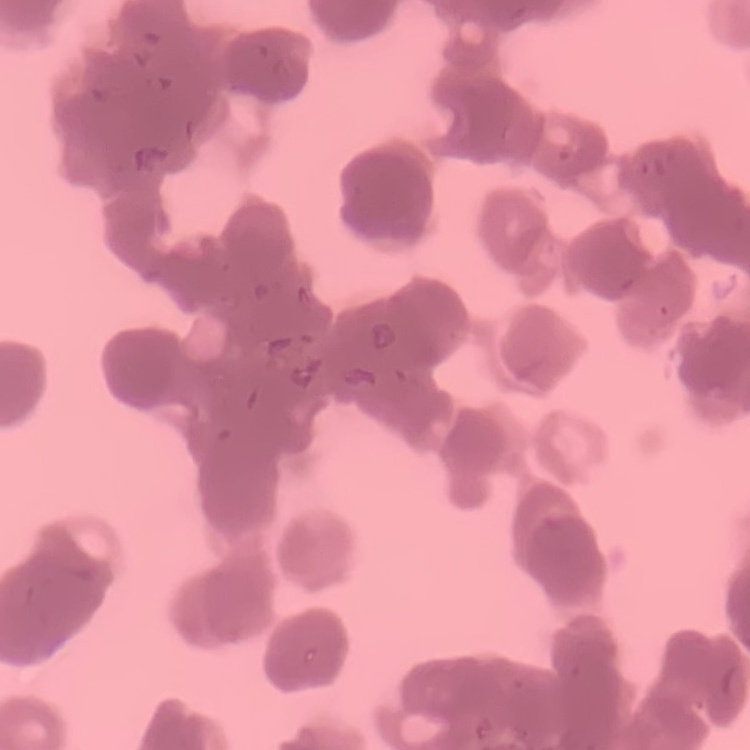
The erythrocytes exhibit rouleaux formation. Thin peripheral smear. Stained with either Field's or Giemsa. Square crop of a larger photomicrograph.